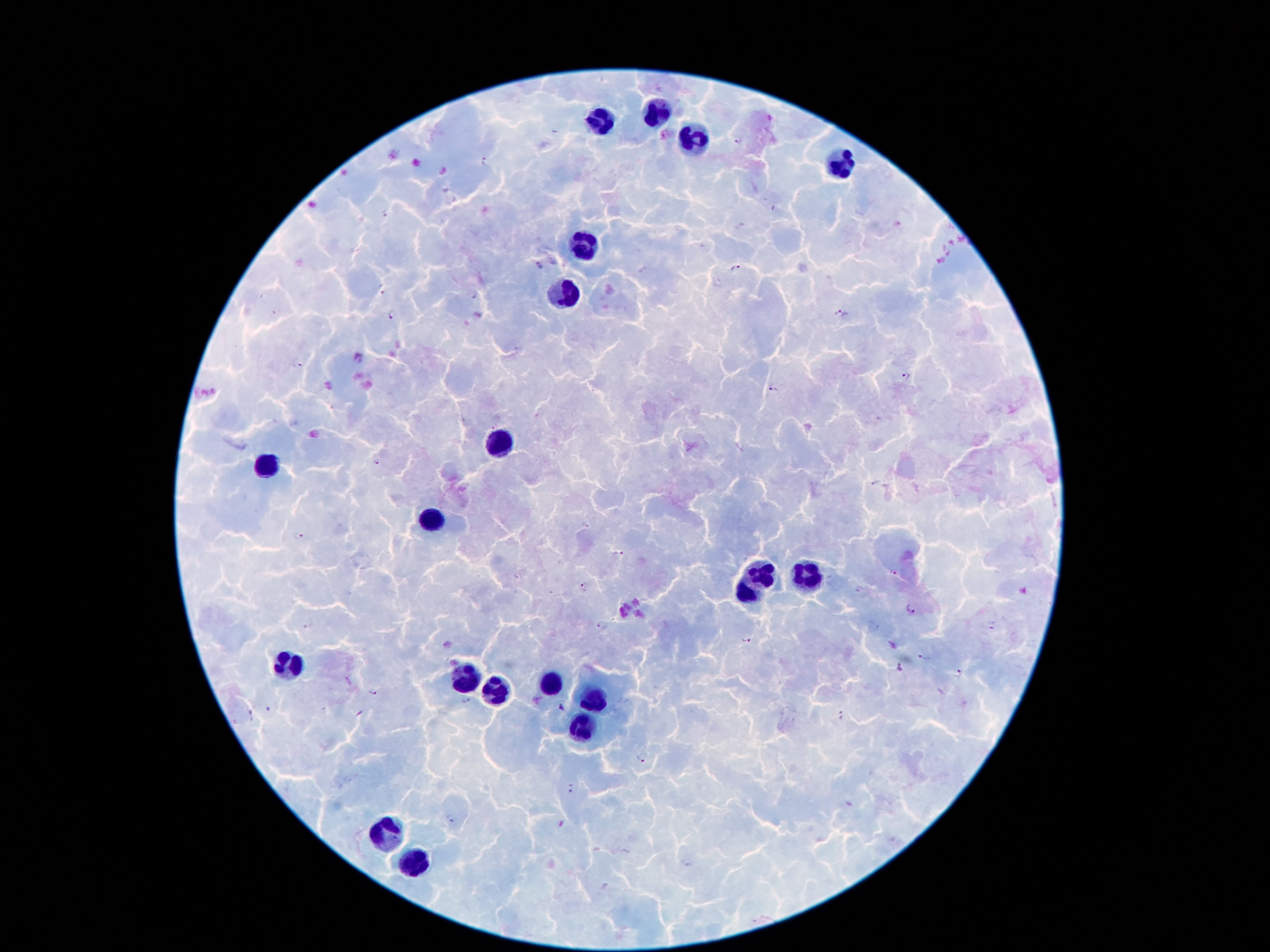

coordinate format = approximate centers as [x, y] in pixels
leukocyte locations = [659, 112], [602, 119], [696, 140], [841, 163], [587, 243], [564, 295], [505, 442], [266, 466], [430, 521], [763, 574], [805, 575], [743, 594], [291, 666], [465, 677], [549, 685], [495, 692], [590, 703], [584, 726], [385, 837], [410, 863]
Plasmodium parasite locations = [741, 141], [484, 161], [387, 215], [539, 267], [735, 268], [383, 290], [392, 314], [840, 315], [298, 364], [906, 377], [774, 389], [378, 463], [877, 481], [297, 536], [616, 555], [894, 573], [581, 589], [910, 608], [601, 626], [992, 626], [310, 627], [746, 640], [923, 658], [901, 666], [959, 673], [372, 693], [466, 703], [560, 708], [269, 709], [843, 716], [254, 717], [644, 759], [573, 789], [451, 820]
field of view = single
patient malaria status = infected with Plasmodium falciparum
capture = smartphone camera through the microscope eyepiece
image size = 1270×952 pixels
stain = Giemsa
magnification = 100x
preparation = thick blood smear